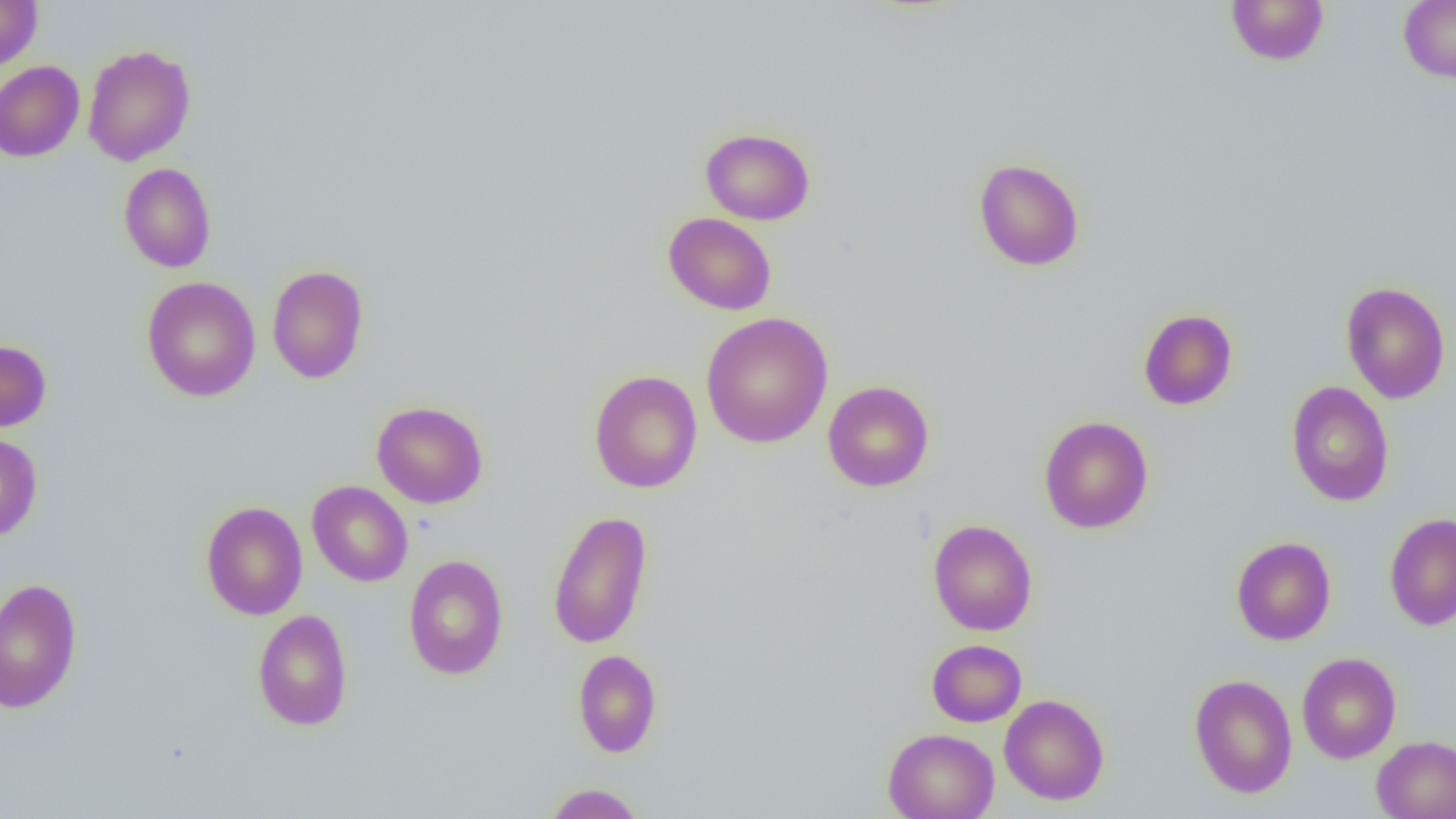

Approximate bounding boxes as (x1,y1)-(x2,y2) corner pairs in pixels. Uninfected red blood cell locations: (0,0)-(42,71), (1225,0)-(1330,66), (1398,0)-(1456,82), (82,44)-(196,166), (0,61)-(85,162), (700,127)-(815,225), (973,158)-(1085,272), (119,162)-(217,273), (663,212)-(776,315), (267,265)-(368,384), (141,276)-(261,402), (1340,281)-(1451,404), (1138,308)-(1238,411), (701,312)-(833,448), (0,339)-(51,433), (588,369)-(703,493), (822,380)-(934,492), (1285,381)-(1394,506), (372,400)-(488,508), (1039,416)-(1154,533), (0,432)-(43,542), (307,480)-(413,587), (201,501)-(307,620), (547,510)-(653,650), (1385,512)-(1456,631), (927,519)-(1037,636), (1231,537)-(1336,645), (403,554)-(509,680), (0,577)-(83,713), (252,609)-(353,731), (927,639)-(1027,727), (573,649)-(662,758), (1296,652)-(1401,763), (1189,674)-(1298,798), (999,694)-(1109,805), (882,728)-(999,819), (1371,735)-(1456,819), (544,782)-(645,819). Slide-level diagnosis: negative for blood parasites. Thin blood smear. Single field of view. Image is 1456×819 pixels. Captured at 1000x magnification. Optical microscopy.